Assess this cell for malaria.
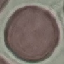

Uninfected.

Giemsa stain. Thin smear of blood. Photographed with a smartphone camera at the microscope eyepiece. Cell patch, automatically extracted from a larger field of view and resized to 64 × 64 pixels.